State which parasite is depicted.
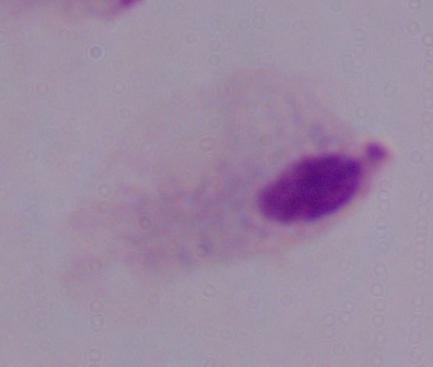

This is a trichomonad.

Summary:
  - Modality: photomicrograph
  - Magnification: 1000x